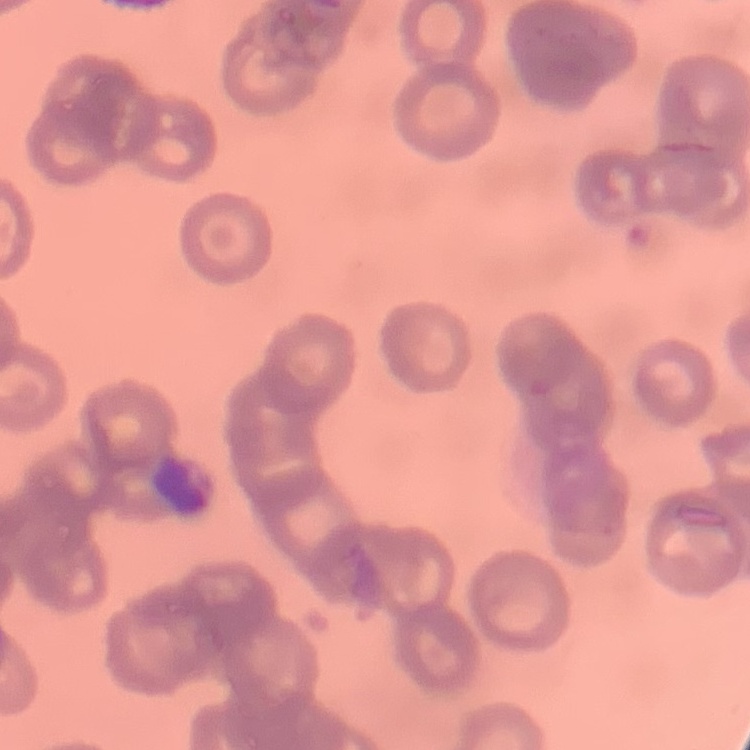

The red blood cells exhibit rouleaux formation. One tile cut from a larger photomicrograph. Thin peripheral smear. Field's or Giemsa stain.